Locate and identify every blood parasite.
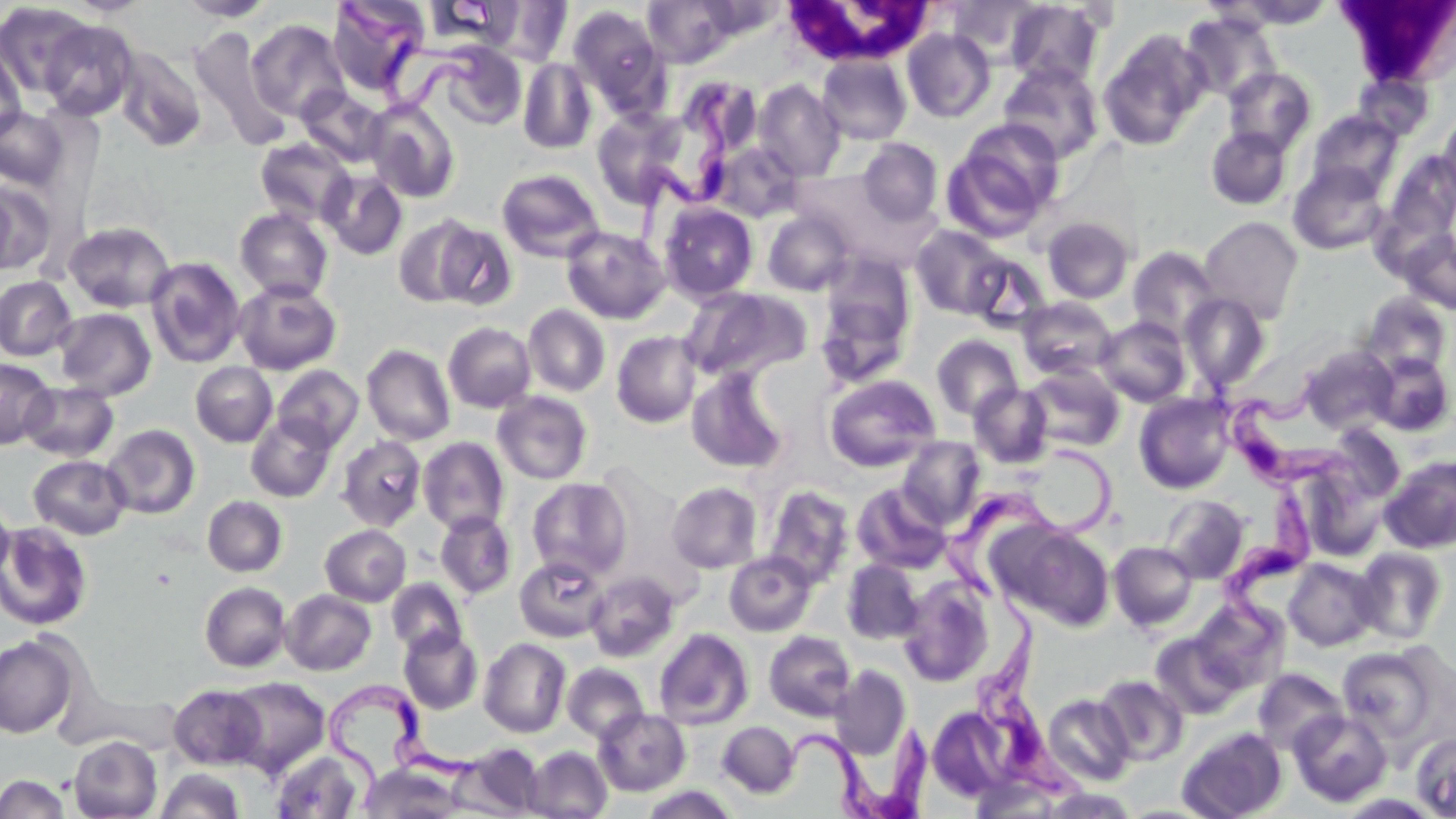
Approximate bounding boxes as [x1, y1, x2, y2] in pixels.
Trypanosoma brucei: [338, 0, 491, 116], [627, 84, 739, 254], [1215, 360, 1374, 510], [938, 439, 1125, 613], [1216, 479, 1317, 668], [973, 582, 1090, 801], [319, 682, 489, 806], [776, 721, 936, 819].
No Plasmodium falciparum, Plasmodium ovale, Plasmodium malariae, Plasmodium vivax, or Babesia divergens observed.

slide-level diagnosis = Trypanosoma brucei
magnification = 1000x
field of view = single
stain = May-Grünwald-Giemsa
modality = optical microscopy
image size = 1456×819 pixels
preparation = thin blood smear
white blood cell locations = approximate bounding boxes as [x1, y1, x2, y2] in pixels: [1338, 0, 1456, 87], [782, 1, 935, 67]
uninfected red blood cell locations = approximate bounding boxes as [x1, y1, x2, y2] in pixels: [176, 0, 276, 22], [327, 0, 430, 98], [642, 0, 736, 67], [948, 0, 1042, 63], [487, 1, 573, 66], [1005, 1, 1105, 87], [1224, 1, 1334, 30], [0, 2, 93, 99], [568, 5, 668, 115], [1181, 12, 1281, 103], [247, 18, 350, 123], [39, 19, 139, 121], [190, 28, 291, 150], [902, 28, 995, 122], [1098, 31, 1210, 150], [436, 42, 528, 130], [0, 46, 26, 143], [114, 47, 207, 152], [817, 55, 912, 145], [518, 57, 597, 154], [998, 63, 1105, 163], [1223, 67, 1316, 155], [1353, 70, 1433, 140], [753, 79, 845, 181], [297, 86, 388, 167], [365, 101, 460, 203], [646, 104, 732, 207], [0, 107, 69, 189], [592, 108, 688, 207], [1306, 110, 1404, 198], [1438, 114, 1456, 203], [956, 117, 1065, 221], [1205, 127, 1292, 210], [255, 138, 355, 226], [858, 138, 943, 225], [708, 142, 804, 222], [1386, 152, 1456, 239], [1288, 162, 1390, 255], [496, 168, 605, 263], [320, 170, 408, 260], [791, 170, 911, 258], [0, 181, 54, 275], [658, 202, 759, 302], [235, 208, 333, 302], [762, 210, 853, 296], [394, 214, 482, 308], [1199, 216, 1303, 324], [1042, 217, 1134, 304], [63, 221, 176, 312], [432, 221, 517, 310], [911, 225, 1009, 318], [561, 226, 670, 324], [1399, 228, 1456, 314], [1127, 245, 1223, 344], [964, 251, 1052, 333], [145, 257, 245, 368], [815, 264, 916, 386], [0, 275, 77, 361], [234, 281, 342, 375], [680, 285, 812, 382], [1180, 293, 1270, 392], [1360, 293, 1453, 379], [1016, 297, 1117, 380], [524, 304, 610, 397], [54, 308, 157, 400], [1095, 317, 1191, 407], [443, 322, 536, 412], [612, 330, 701, 428], [931, 334, 1023, 421], [362, 344, 455, 446], [1299, 345, 1396, 434], [1367, 352, 1454, 437], [0, 357, 56, 449], [190, 362, 277, 447], [273, 364, 363, 451], [1023, 364, 1124, 452], [687, 366, 789, 473], [824, 375, 940, 471], [20, 382, 119, 462], [969, 384, 1053, 468], [492, 391, 593, 484], [1134, 392, 1236, 493], [246, 414, 336, 502], [102, 424, 200, 519], [337, 436, 427, 531], [418, 436, 510, 535], [898, 436, 985, 529], [29, 455, 131, 540], [1381, 456, 1456, 553], [1303, 472, 1388, 562], [527, 477, 632, 580], [667, 481, 762, 573], [852, 483, 953, 574], [763, 485, 855, 589], [1160, 495, 1249, 583], [0, 496, 15, 587], [202, 496, 287, 577], [435, 511, 516, 599], [0, 522, 93, 631], [1001, 523, 1114, 630], [320, 525, 411, 606], [1109, 541, 1198, 631], [1353, 547, 1447, 644], [724, 551, 817, 637], [515, 556, 608, 642], [1284, 558, 1379, 651], [842, 559, 923, 644], [586, 571, 679, 661], [387, 579, 466, 655], [898, 580, 995, 687], [199, 581, 291, 672], [281, 589, 376, 675], [1192, 598, 1289, 693], [399, 627, 482, 714], [654, 628, 754, 730], [764, 630, 856, 721], [1151, 633, 1245, 720], [0, 634, 78, 738], [479, 637, 571, 738], [1337, 644, 1447, 745], [562, 662, 649, 744], [830, 665, 911, 759], [1253, 668, 1348, 755], [1095, 675, 1188, 765], [225, 676, 330, 776], [168, 684, 267, 769], [63, 689, 182, 754], [1043, 694, 1134, 785], [926, 706, 1018, 803], [594, 708, 690, 796], [1289, 709, 1393, 807], [717, 721, 800, 797], [1177, 727, 1287, 819], [1411, 731, 1456, 817], [69, 735, 162, 819], [461, 743, 545, 816], [525, 746, 612, 818], [271, 749, 365, 818], [361, 764, 462, 818], [156, 768, 244, 819], [0, 773, 69, 819], [640, 785, 739, 818], [1337, 793, 1444, 818]